Name the blood parasite species.
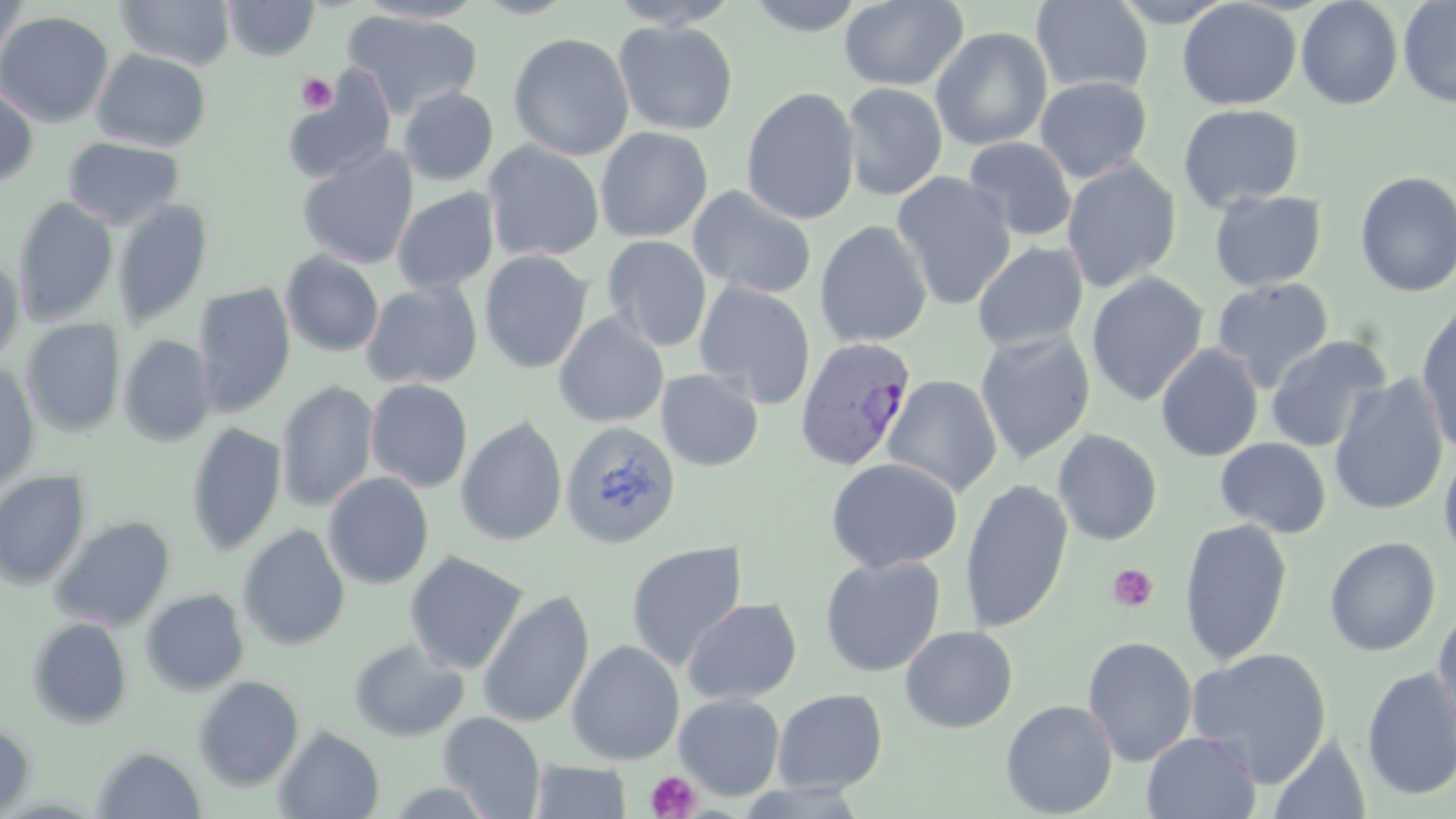

Plasmodium vivax.

Approximate bounding boxes as (x1,y1)-(x2,y2) corner pairs in pixels. Plasmodium vivax-infected red blood cell locations: (794,336)-(919,471). Uninfected red blood cell locations: (0,0)-(29,68), (115,0)-(236,69), (222,0)-(320,61), (471,0)-(579,19), (607,0)-(741,30), (744,0)-(867,36), (839,0)-(969,91), (1177,0)-(1301,110), (1296,0)-(1403,110), (1398,0)-(1456,108), (353,1)-(490,24), (1031,1)-(1153,95), (342,9)-(483,119), (0,10)-(114,128), (613,20)-(739,136), (930,26)-(1053,151), (508,32)-(634,161), (92,49)-(212,151), (281,68)-(396,184), (1034,76)-(1153,183), (841,82)-(948,201), (0,85)-(39,188), (740,86)-(860,224), (398,87)-(499,186), (1178,103)-(1304,212), (595,126)-(713,243), (63,137)-(185,229), (964,137)-(1078,241), (483,141)-(605,263), (297,146)-(418,269), (1062,159)-(1182,293), (891,171)-(1016,310), (1354,171)-(1456,298), (687,185)-(818,300), (391,188)-(500,294), (1209,190)-(1327,291), (13,196)-(119,327), (112,199)-(213,330), (815,220)-(933,348), (602,235)-(712,352), (973,241)-(1088,351), (478,250)-(594,374), (280,251)-(385,357), (0,254)-(25,366), (1085,272)-(1208,407), (1212,277)-(1334,392), (360,280)-(483,389), (693,280)-(816,409), (193,282)-(296,417), (1185,304)-(1308,442), (1416,305)-(1456,456), (554,312)-(669,427), (21,319)-(125,437), (974,330)-(1096,464), (1265,334)-(1392,453), (118,335)-(216,446), (1155,344)-(1263,463), (0,361)-(40,494), (656,368)-(764,471), (1328,374)-(1450,517), (881,375)-(1002,498), (365,378)-(474,493), (276,380)-(378,513), (456,415)-(568,546), (561,422)-(682,549), (185,423)-(286,557), (1052,429)-(1163,545), (1215,437)-(1331,538), (1438,446)-(1456,565), (825,457)-(963,573), (0,470)-(90,589), (322,472)-(434,589), (960,479)-(1073,634), (50,515)-(175,631), (1178,518)-(1293,666), (237,524)-(351,651), (1323,536)-(1441,656), (625,541)-(747,670), (404,550)-(529,675), (819,554)-(946,677), (140,588)-(249,695), (477,589)-(594,728), (682,597)-(802,705), (1433,605)-(1456,743), (27,617)-(132,729), (899,625)-(1018,732), (1081,636)-(1198,767), (347,638)-(469,742), (567,639)-(685,765), (1185,646)-(1333,787), (1361,667)-(1456,801), (192,675)-(305,790), (772,688)-(888,793), (674,693)-(785,800), (1000,699)-(1118,818), (438,711)-(546,818), (0,722)-(35,816), (274,725)-(385,819), (1141,731)-(1262,819), (1269,734)-(1371,818), (92,746)-(207,818), (529,761)-(632,818). Platelet locations: (296,73)-(338,113), (1108,564)-(1159,612), (645,769)-(702,818). Thin blood film. Light microscopy. May-Grünwald-Giemsa-stained preparation. Image is 1456×819 pixels. One field of a larger specimen. Captured at 1000x magnification.